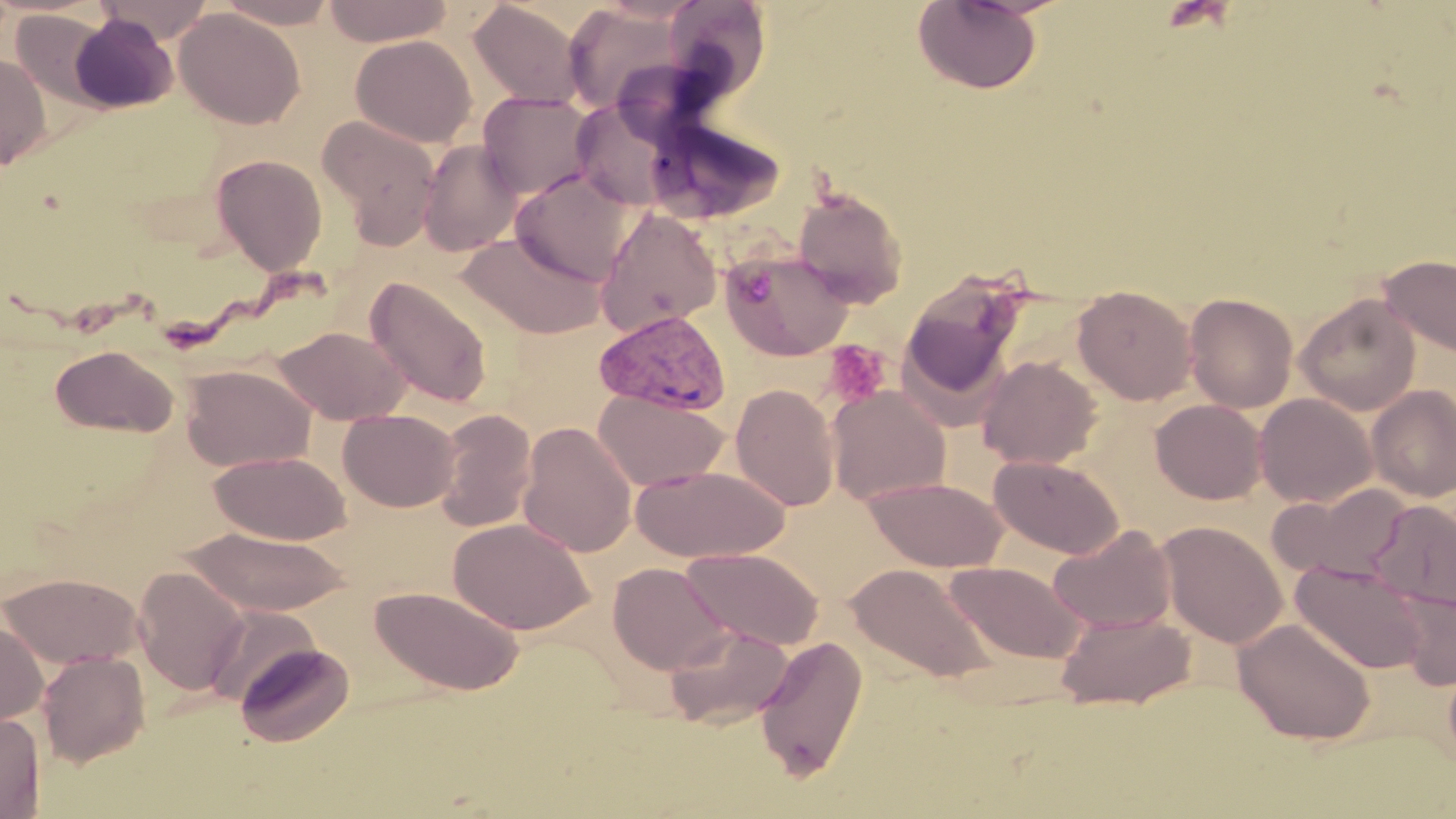

Summary:
  - Coordinate format: approximate bounding boxes as (x1, y1, x2, y2) in pixels
  - Plasmodium vivax-infected red blood cell locations: (593, 309, 730, 415)
  - Platelet locations: (823, 339, 890, 408)
  - Uninfected red blood cell locations: (94, 0, 217, 43), (214, 0, 341, 28), (322, 0, 455, 46), (663, 0, 773, 99), (912, 0, 1043, 94), (468, 2, 584, 107), (564, 4, 685, 115), (173, 8, 305, 129), (10, 10, 114, 110), (69, 15, 178, 113), (351, 35, 477, 147), (0, 52, 52, 171), (477, 92, 598, 200), (570, 99, 677, 212), (317, 115, 441, 245), (644, 119, 785, 225), (418, 140, 524, 257), (210, 152, 328, 275), (511, 169, 636, 286), (792, 188, 908, 306), (595, 207, 722, 337), (458, 231, 607, 339), (721, 249, 854, 362), (1378, 254, 1456, 358), (900, 273, 1025, 404), (365, 276, 494, 409), (1073, 285, 1197, 405), (1184, 293, 1298, 413), (1296, 294, 1421, 415), (273, 325, 410, 425), (50, 345, 179, 437), (976, 355, 1103, 469), (181, 365, 316, 472), (730, 383, 840, 512), (827, 386, 951, 505), (1367, 386, 1456, 502), (594, 389, 731, 491), (1253, 394, 1376, 508), (1150, 399, 1267, 504), (338, 408, 460, 512), (433, 409, 537, 533), (518, 421, 637, 557), (210, 451, 351, 545), (989, 454, 1124, 559), (628, 465, 789, 562), (864, 476, 1008, 572), (1268, 483, 1412, 583), (1371, 501, 1455, 610), (448, 517, 595, 635), (1156, 521, 1286, 648), (1048, 524, 1176, 633), (184, 527, 354, 616), (684, 548, 823, 650), (944, 561, 1086, 664), (1290, 561, 1428, 674), (607, 562, 732, 675), (847, 562, 997, 684), (132, 566, 249, 696), (1, 572, 144, 669), (370, 586, 524, 695), (1393, 590, 1456, 690), (205, 605, 320, 708), (1055, 611, 1196, 710), (1233, 617, 1376, 745), (0, 621, 48, 724), (664, 623, 794, 729), (755, 636, 869, 781), (234, 641, 355, 748), (37, 651, 150, 768), (1443, 654, 1456, 773), (0, 710, 45, 818)
  - Slide-level diagnosis: Plasmodium vivax
  - Magnification: 1000x
  - Preparation: thin blood smear
  - Stain: May-Grünwald-Giemsa
  - Modality: optical microscopy
  - Field of view: one of a larger specimen
  - Image size: 1456×819 pixels